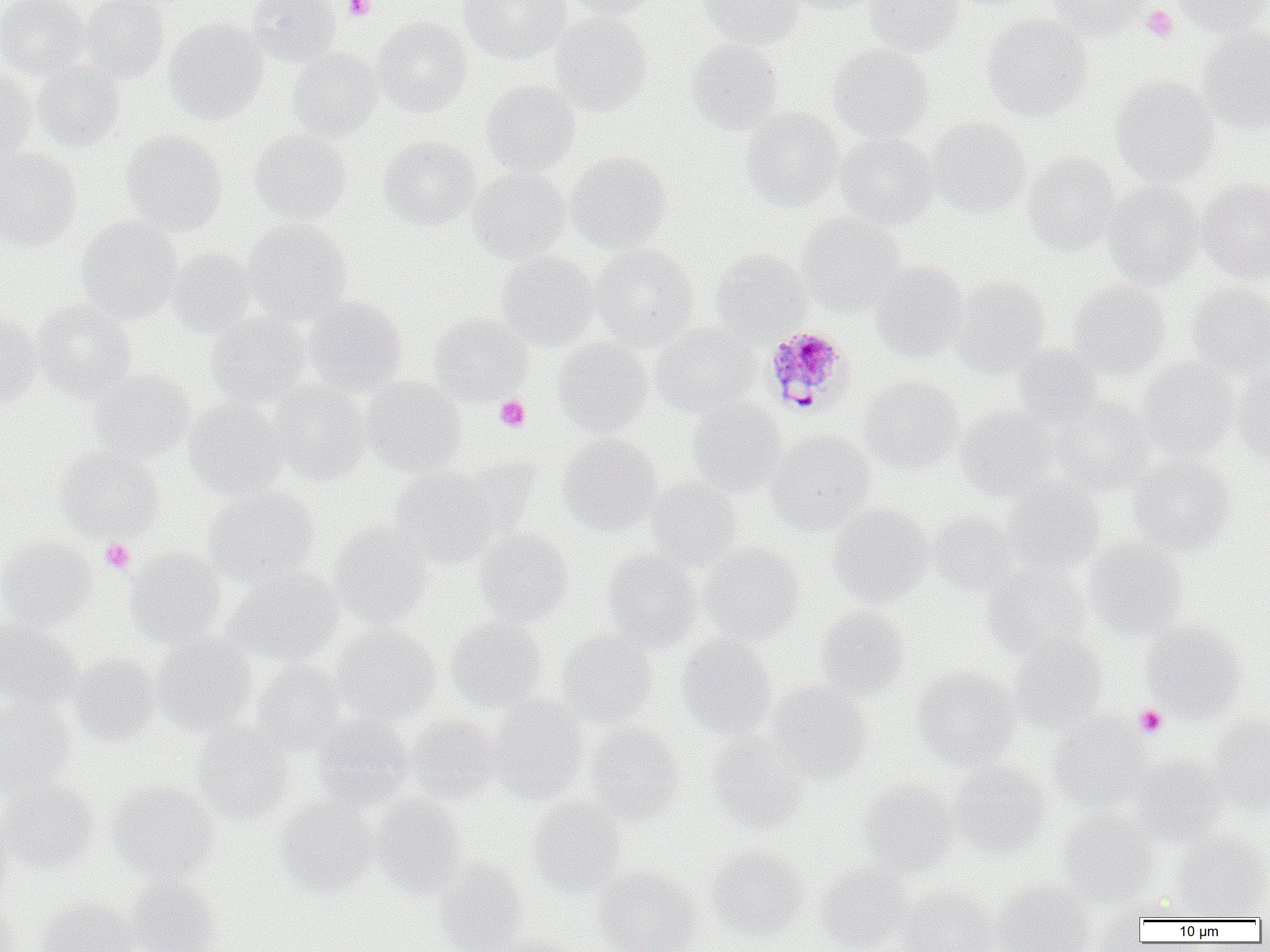
slide_level_diagnosis: Plasmodium malariae
uninfected_red_blood_cell_locations: 'approximate bounding boxes as named x1/y1/x2/y2 corners in pixels: (x1=0, y1=0, x2=90, y2=79), (x1=79, y1=0, x2=169, y2=82), (x1=245, y1=0, x2=341, y2=66), (x1=458, y1=0, x2=571, y2=64), (x1=560, y1=0, x2=659, y2=20), (x1=699, y1=0, x2=804, y2=49), (x1=780, y1=0, x2=884, y2=16), (x1=865, y1=0, x2=962, y2=57), (x1=1042, y1=0, x2=1151, y2=38), (x1=1170, y1=0, x2=1269, y2=37), (x1=550, y1=12, x2=651, y2=116), (x1=983, y1=14, x2=1092, y2=121), (x1=372, y1=17, x2=472, y2=117), (x1=164, y1=19, x2=268, y2=124), (x1=1197, y1=28, x2=1270, y2=134), (x1=686, y1=39, x2=784, y2=134), (x1=828, y1=43, x2=934, y2=143), (x1=288, y1=47, x2=382, y2=141), (x1=32, y1=60, x2=125, y2=152), (x1=0, y1=67, x2=36, y2=162), (x1=1, y1=67, x2=87, y2=157), (x1=1112, y1=76, x2=1219, y2=187), (x1=481, y1=79, x2=581, y2=176), (x1=740, y1=107, x2=842, y2=211), (x1=927, y1=117, x2=1030, y2=218), (x1=122, y1=129, x2=227, y2=236), (x1=250, y1=130, x2=351, y2=224), (x1=835, y1=133, x2=938, y2=229), (x1=380, y1=136, x2=481, y2=230), (x1=0, y1=148, x2=82, y2=252), (x1=567, y1=151, x2=671, y2=254), (x1=1022, y1=153, x2=1121, y2=256), (x1=467, y1=168, x2=570, y2=263), (x1=1198, y1=178, x2=1270, y2=284), (x1=1103, y1=182, x2=1205, y2=287), (x1=796, y1=213, x2=904, y2=315), (x1=76, y1=216, x2=182, y2=324), (x1=243, y1=218, x2=351, y2=324), (x1=591, y1=244, x2=699, y2=350), (x1=167, y1=247, x2=257, y2=339), (x1=710, y1=250, x2=811, y2=341), (x1=497, y1=251, x2=599, y2=349), (x1=870, y1=260, x2=969, y2=362), (x1=952, y1=277, x2=1050, y2=377), (x1=1068, y1=281, x2=1169, y2=380), (x1=1186, y1=284, x2=1270, y2=379), (x1=305, y1=297, x2=407, y2=395), (x1=34, y1=300, x2=136, y2=400), (x1=0, y1=312, x2=41, y2=404), (x1=206, y1=313, x2=312, y2=408), (x1=430, y1=313, x2=532, y2=403), (x1=651, y1=324, x2=760, y2=417), (x1=552, y1=337, x2=652, y2=436), (x1=1013, y1=344, x2=1103, y2=429), (x1=1137, y1=358, x2=1238, y2=461), (x1=90, y1=370, x2=194, y2=464), (x1=1232, y1=370, x2=1270, y2=467), (x1=861, y1=377, x2=963, y2=473), (x1=363, y1=378, x2=467, y2=476), (x1=270, y1=381, x2=371, y2=484), (x1=1052, y1=396, x2=1156, y2=495), (x1=687, y1=398, x2=787, y2=496), (x1=183, y1=399, x2=288, y2=499), (x1=956, y1=405, x2=1058, y2=498), (x1=767, y1=431, x2=875, y2=534), (x1=557, y1=434, x2=662, y2=535), (x1=55, y1=445, x2=164, y2=542), (x1=1129, y1=455, x2=1235, y2=555), (x1=390, y1=466, x2=501, y2=567), (x1=645, y1=478, x2=742, y2=570), (x1=1002, y1=480, x2=1104, y2=574), (x1=204, y1=487, x2=320, y2=587), (x1=827, y1=504, x2=932, y2=607), (x1=928, y1=512, x2=1019, y2=594), (x1=330, y1=522, x2=432, y2=629), (x1=474, y1=529, x2=573, y2=625), (x1=0, y1=536, x2=97, y2=631), (x1=1084, y1=538, x2=1188, y2=639), (x1=700, y1=543, x2=804, y2=643), (x1=126, y1=548, x2=226, y2=648), (x1=603, y1=551, x2=702, y2=651), (x1=984, y1=564, x2=1090, y2=658), (x1=222, y1=567, x2=343, y2=667), (x1=816, y1=607, x2=909, y2=700), (x1=447, y1=617, x2=547, y2=712), (x1=0, y1=621, x2=83, y2=713), (x1=1142, y1=622, x2=1245, y2=719), (x1=331, y1=625, x2=441, y2=725), (x1=558, y1=631, x2=657, y2=729), (x1=152, y1=633, x2=256, y2=737), (x1=677, y1=635, x2=776, y2=738), (x1=1008, y1=636, x2=1106, y2=731), (x1=69, y1=653, x2=160, y2=745), (x1=252, y1=659, x2=347, y2=754), (x1=912, y1=667, x2=1018, y2=770), (x1=767, y1=682, x2=872, y2=783), (x1=488, y1=696, x2=588, y2=805), (x1=0, y1=700, x2=75, y2=797), (x1=312, y1=713, x2=412, y2=807), (x1=405, y1=714, x2=502, y2=802), (x1=1049, y1=714, x2=1152, y2=812), (x1=1209, y1=714, x2=1270, y2=814), (x1=587, y1=722, x2=684, y2=824), (x1=192, y1=724, x2=294, y2=825), (x1=706, y1=734, x2=808, y2=833), (x1=1130, y1=755, x2=1230, y2=845), (x1=949, y1=762, x2=1051, y2=857), (x1=0, y1=779, x2=98, y2=873), (x1=108, y1=780, x2=219, y2=883), (x1=858, y1=781, x2=955, y2=877), (x1=373, y1=795, x2=467, y2=899), (x1=276, y1=797, x2=378, y2=897), (x1=528, y1=797, x2=627, y2=898), (x1=1058, y1=809, x2=1157, y2=906), (x1=0, y1=815, x2=13, y2=906), (x1=1171, y1=834, x2=1269, y2=920), (x1=706, y1=846, x2=808, y2=943), (x1=433, y1=858, x2=528, y2=952), (x1=815, y1=864, x2=912, y2=952), (x1=595, y1=867, x2=700, y2=952), (x1=125, y1=875, x2=220, y2=952), (x1=993, y1=881, x2=1095, y2=952), (x1=898, y1=888, x2=999, y2=952), (x1=35, y1=897, x2=139, y2=952), (x1=0, y1=899, x2=20, y2=952), (x1=488, y1=933, x2=587, y2=952)'
platelet_locations: 'approximate bounding boxes as named x1/y1/x2/y2 corners in pixels: (x1=343, y1=0, x2=375, y2=21), (x1=1141, y1=5, x2=1178, y2=42), (x1=494, y1=395, x2=530, y2=431), (x1=100, y1=538, x2=134, y2=573), (x1=1134, y1=705, x2=1167, y2=738)'
modality: light microscopy
field_of_view: single
image_size: 1270×952 pixels
magnification: 1000x
preparation: thin blood smear
plasmodium_malariae_infected_red_blood_cell_locations: 'approximate bounding boxes as named x1/y1/x2/y2 corners in pixels: (x1=769, y1=325, x2=864, y2=417)'